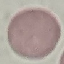
result = no malaria parasites detected
stain = Giemsa
preparation = thin blood smear
capture = smartphone through the microscope eyepiece
image type = automatically extracted cell patch, resized to 64 × 64 pixels